Report the malaria status of this cell.
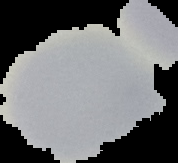

It is uninfected.

preparation: thin blood smear
image_type: segmented cell region on a black background
image_size: 178×163 pixels